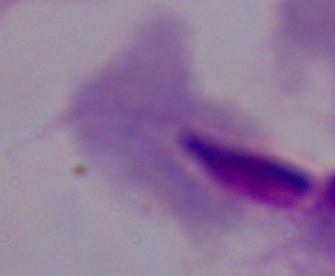
Photomicrograph. A trichomonad is shown. Captured at 1000x magnification.